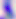
modality: micrograph
identification: Toxoplasma gondii
magnification: 400x